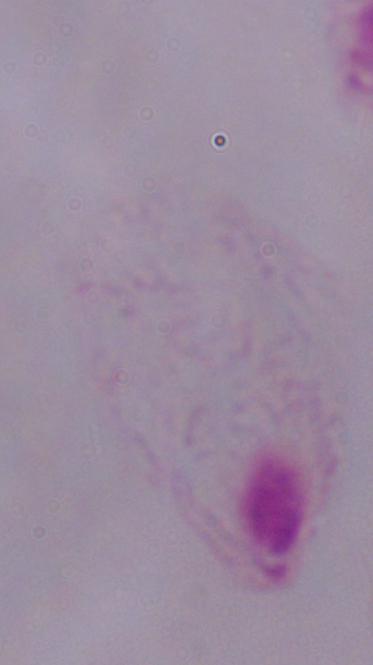
Summary:
  - Modality: photomicrograph
  - Identification: trichomonad
  - Magnification: 1000x